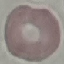
Malaria status: uninfected. Thin smear of blood. Giemsa stain. Automatically extracted cell patch, resized to 64 × 64 pixels. Photographed with a smartphone camera at the microscope eyepiece.